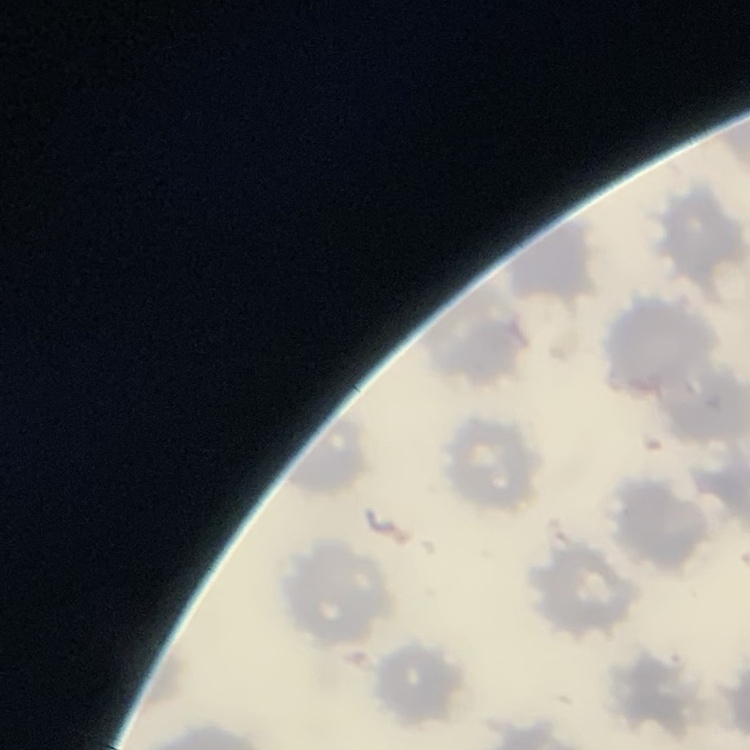

Summary:
  - Red blood cell morphology: no rouleaux formation
  - Preparation: thin blood film
  - Stain: Field's or Giemsa
  - Image type: square crop of a larger photomicrograph